Outline each blood parasite and name the species.
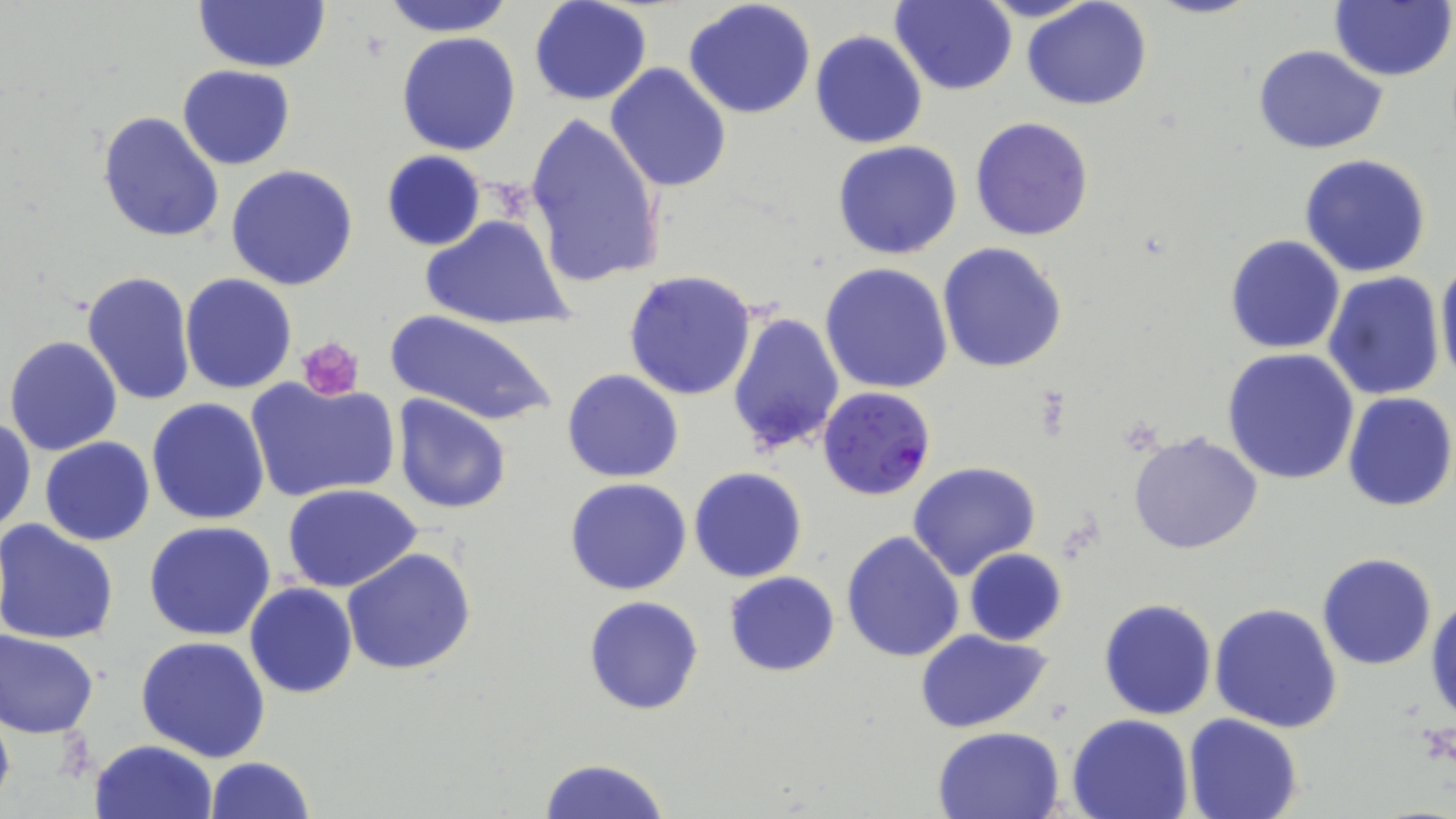
Approximate bounding boxes as (x1, y1, x2, y2) in pixels.
Plasmodium falciparum-infected red blood cells: (818, 384, 937, 501).
No Plasmodium ovale, Plasmodium malariae, Plasmodium vivax, Babesia divergens, or Trypanosoma brucei observed.

slide-level diagnosis = Plasmodium falciparum
preparation = thin blood smear
magnification = 1000x
stain = May-Grünwald-Giemsa
platelet locations = approximate bounding boxes as (x1, y1, x2, y2) in pixels: (300, 336, 364, 400)
uninfected red blood cell locations = approximate bounding boxes as (x1, y1, x2, y2) in pixels: (194, 0, 331, 73), (381, 0, 513, 37), (529, 0, 653, 105), (889, 0, 1018, 95), (1021, 0, 1153, 111), (1329, 0, 1456, 82), (683, 1, 817, 120), (810, 30, 927, 149), (396, 32, 523, 156), (1250, 44, 1390, 154), (605, 63, 731, 193), (177, 66, 295, 169), (97, 110, 224, 245), (523, 113, 663, 288), (970, 116, 1094, 242), (832, 140, 963, 260), (380, 150, 488, 252), (1300, 153, 1433, 278), (226, 164, 357, 291), (421, 214, 572, 330), (1224, 236, 1345, 354), (938, 242, 1069, 373), (1435, 256, 1456, 389), (820, 261, 953, 395), (624, 269, 758, 399), (81, 270, 196, 407), (1322, 270, 1447, 402), (179, 274, 297, 394), (726, 309, 846, 458), (381, 310, 559, 426), (4, 336, 124, 456), (1221, 346, 1360, 486), (562, 370, 683, 482), (246, 379, 399, 501), (1341, 391, 1456, 512), (391, 396, 511, 514), (147, 398, 271, 523), (0, 413, 36, 542), (1127, 430, 1264, 556), (39, 437, 154, 544), (907, 461, 1040, 581), (689, 467, 809, 583), (565, 478, 692, 595), (282, 484, 422, 593), (0, 519, 121, 644), (144, 520, 277, 641), (841, 531, 965, 664), (342, 548, 477, 677), (963, 548, 1068, 647), (1317, 553, 1438, 671), (723, 571, 840, 677), (245, 583, 358, 699), (1427, 594, 1456, 727), (583, 596, 704, 715), (1099, 598, 1216, 720), (1209, 602, 1343, 733), (913, 627, 1056, 733), (1, 629, 100, 738), (135, 636, 271, 761), (0, 695, 16, 817), (1184, 712, 1304, 818), (1066, 714, 1194, 819), (932, 726, 1065, 818), (89, 739, 218, 819), (205, 756, 314, 818), (535, 757, 672, 819)
field of view = one of a larger specimen
image size = 1456×819 pixels
modality = light microscopy